Name the parasite shown.
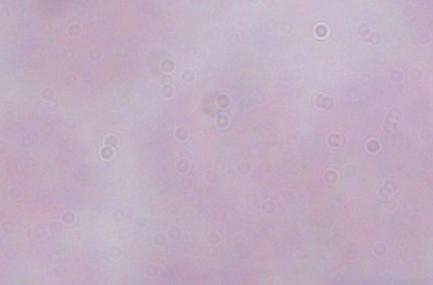
This is a trypanosome.

magnification = 1000x
modality = photomicrograph